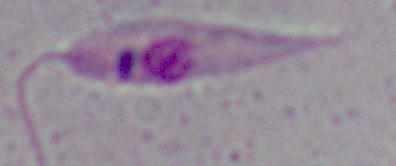 Photomicrograph. A Leishmania parasite is seen. Captured at 1000x magnification.